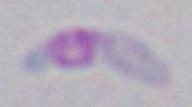
Micrograph. Toxoplasma gondii is seen. Captured at 1000x magnification.